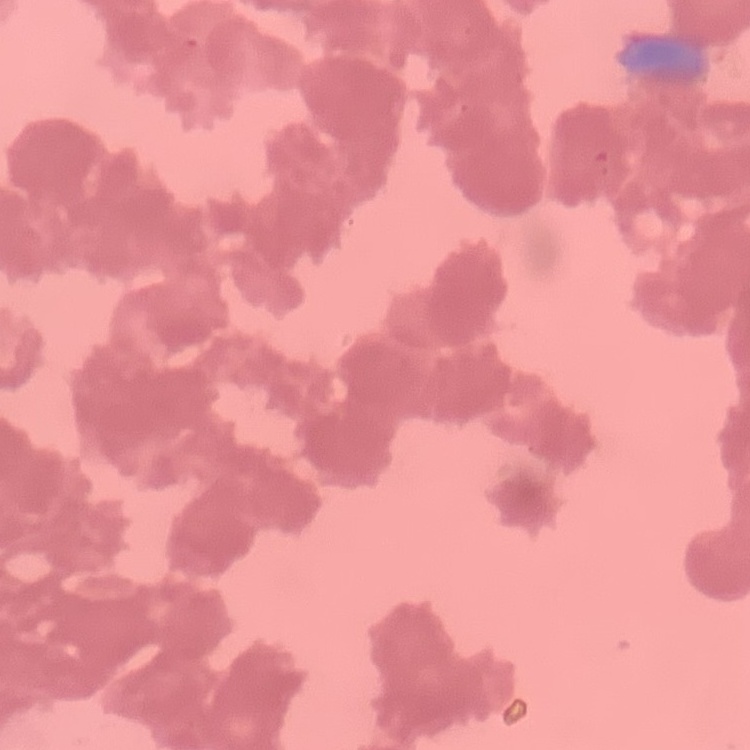
{
  "erythrocyte_morphology": "rouleaux formation",
  "stain": "Field's or Giemsa",
  "preparation": "thin blood film",
  "image_type": "one tile cut from a larger photomicrograph"
}